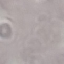

malaria status = uninfected
image type = automatically extracted cell patch, resized to 64 × 64 pixels
capture = smartphone camera at the microscope eyepiece
preparation = thin smear
stain = Giemsa